Identify the preparation type.
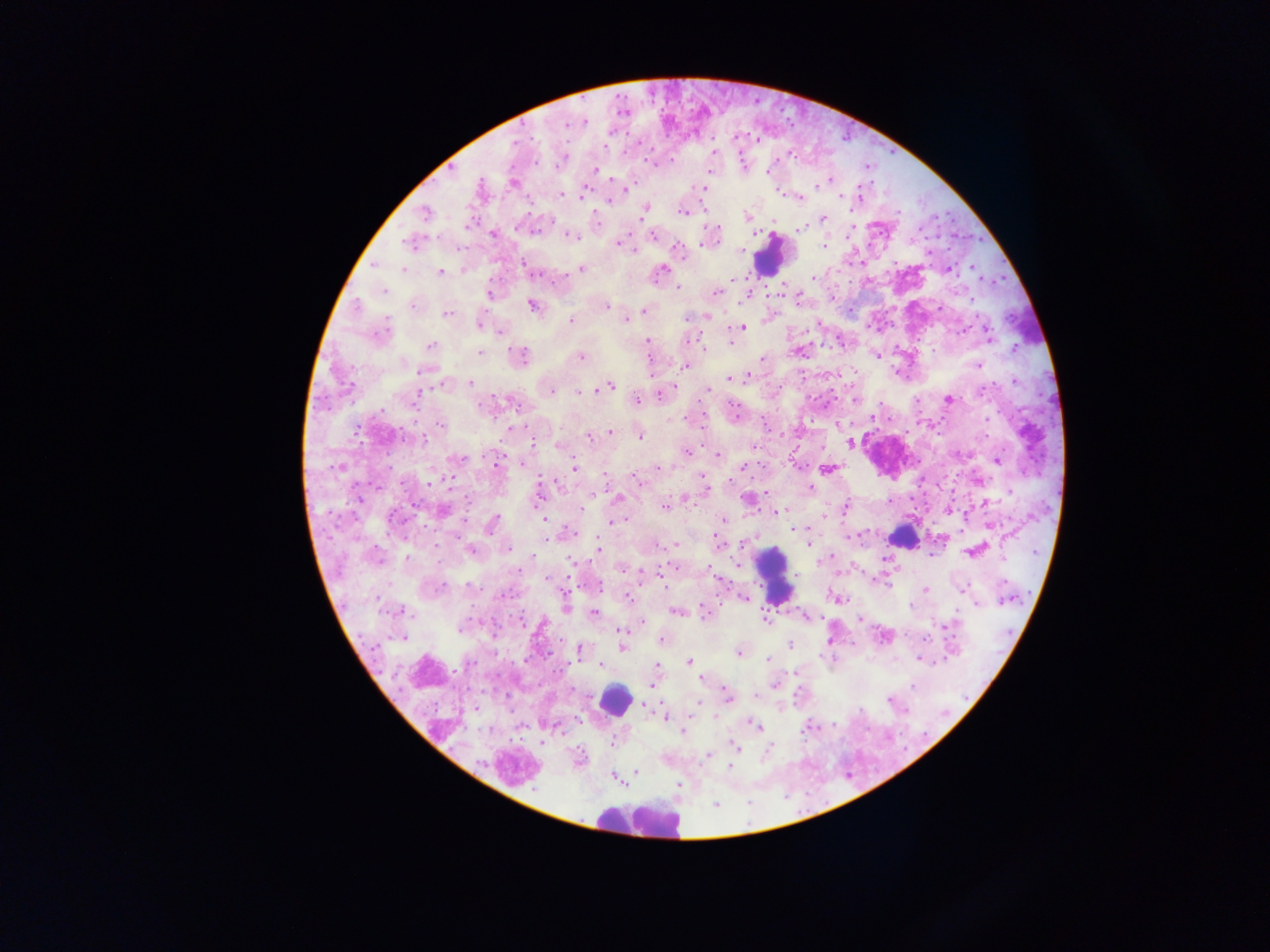
Thick blood smear.

Approximate centers as {x, y} in pixels.
Summary:
  - Leukocyte locations: {771, 254}, {900, 537}, {774, 574}, {615, 699}, {636, 819}
  - Malaria parasite locations: {584, 120}, {567, 124}, {606, 146}, {713, 152}, {649, 162}, {594, 170}, {768, 172}, {512, 183}, {629, 186}, {816, 186}, {701, 188}, {626, 190}, {584, 193}, {779, 193}, {562, 195}, {840, 196}, {799, 197}, {859, 197}, {608, 201}, {647, 208}, {683, 213}, {425, 214}, {746, 216}, {642, 218}, {824, 218}, {469, 224}, {801, 229}, {535, 232}, {493, 234}, {572, 236}, {653, 237}, {407, 242}, {617, 244}, {823, 246}, {678, 250}, {741, 251}, {634, 252}, {523, 263}, {373, 264}, {971, 267}, {581, 269}, {949, 269}, {403, 270}, {662, 270}, {440, 273}, {812, 279}, {671, 284}, {678, 287}, {384, 291}, {716, 292}, {489, 294}, {972, 299}, {531, 305}, {357, 306}, {413, 306}, {607, 306}, {644, 311}, {447, 314}, {687, 317}, {707, 317}, {387, 320}, {571, 320}, {626, 320}, {479, 326}, {743, 327}, {500, 332}, {988, 334}, {648, 341}, {688, 342}, {732, 342}, {431, 346}, {1014, 348}, {703, 349}, {479, 353}, {523, 355}, {876, 356}, {580, 357}, {762, 358}, {977, 365}, {684, 366}, {421, 371}, {729, 379}, {470, 382}, {1015, 382}, {610, 386}, {348, 387}, {596, 390}, {983, 390}, {418, 391}, {552, 391}, {707, 391}, {578, 393}, {660, 395}, {637, 400}, {949, 400}, {733, 407}, {382, 410}, {873, 417}, {987, 419}, {671, 420}, {442, 425}, {357, 432}, {609, 432}, {640, 436}, {589, 438}, {424, 441}, {850, 443}, {534, 444}, {558, 444}, {754, 446}, {687, 452}, {717, 455}, {460, 459}, {496, 462}, {998, 462}, {521, 463}, {743, 467}, {337, 468}, {574, 468}, {658, 468}, {827, 469}, {605, 475}, {702, 476}, {638, 481}, {730, 481}, {451, 482}, {429, 483}, {559, 485}, {811, 488}, {619, 498}, {686, 499}, {467, 500}, {664, 507}, {846, 507}, {582, 508}, {782, 510}, {443, 511}, {777, 512}, {393, 517}, {824, 517}, {544, 520}, {620, 520}, {722, 520}, {612, 523}, {491, 526}, {988, 526}, {793, 529}, {573, 532}, {715, 538}, {545, 540}, {744, 544}, {809, 544}, {675, 546}, {598, 548}, {470, 549}, {509, 550}, {406, 557}, {379, 559}, {570, 561}, {737, 565}, {674, 566}, {622, 569}, {641, 570}, {546, 579}, {663, 585}, {468, 586}, {441, 588}, {601, 588}, {925, 589}, {964, 589}, {504, 595}, {628, 598}, {839, 599}, {1006, 599}, {976, 604}, {910, 605}, {401, 611}, {676, 612}, {593, 613}, {705, 613}, {860, 619}, {764, 620}, {522, 621}, {642, 622}, {948, 628}, {460, 629}, {620, 631}, {622, 637}, {402, 638}, {662, 640}, {790, 645}, {622, 648}, {579, 650}, {739, 652}, {768, 659}, {920, 660}, {689, 662}, {470, 663}, {601, 665}, {657, 665}, {700, 678}, {652, 684}, {775, 685}, {914, 686}, {727, 695}, {756, 696}, {890, 700}, {696, 703}, {665, 716}, {715, 716}, {755, 725}, {806, 728}, {683, 732}, {543, 742}, {613, 744}, {735, 746}, {707, 756}, {730, 768}, {636, 771}, {616, 778}, {680, 784}
  - Image size: 1270×952 pixels
  - Country: Ghana
  - Capture: mobile-phone photograph through a microscope
  - Field of view: single